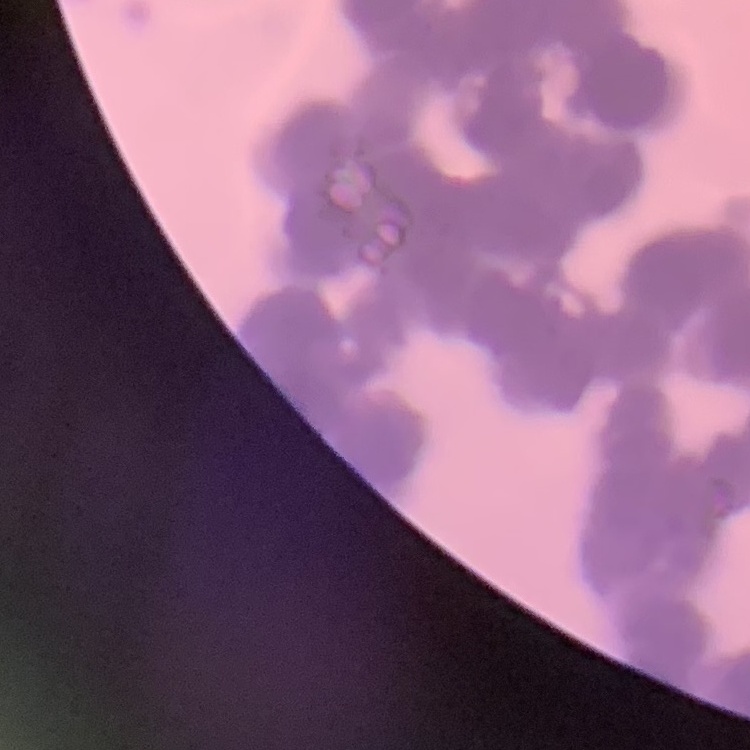

The red blood cells exhibit rouleaux formation. Field's or Giemsa stain. Thin peripheral smear. Square crop of a larger photomicrograph.